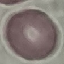

Result: negative for malaria parasites. Cell patch, automatically extracted from a larger field of view and resized to 64 × 64 pixels. Giemsa stain. Acquired by smartphone through the microscope eyepiece. Thin blood smear.